Assess this cell for malaria.
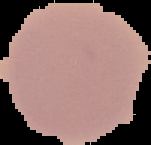

Uninfected.

Cell region segmented out of the field of view; the surrounding area is masked to black. Image is 151×145 pixels. From a thin blood film.